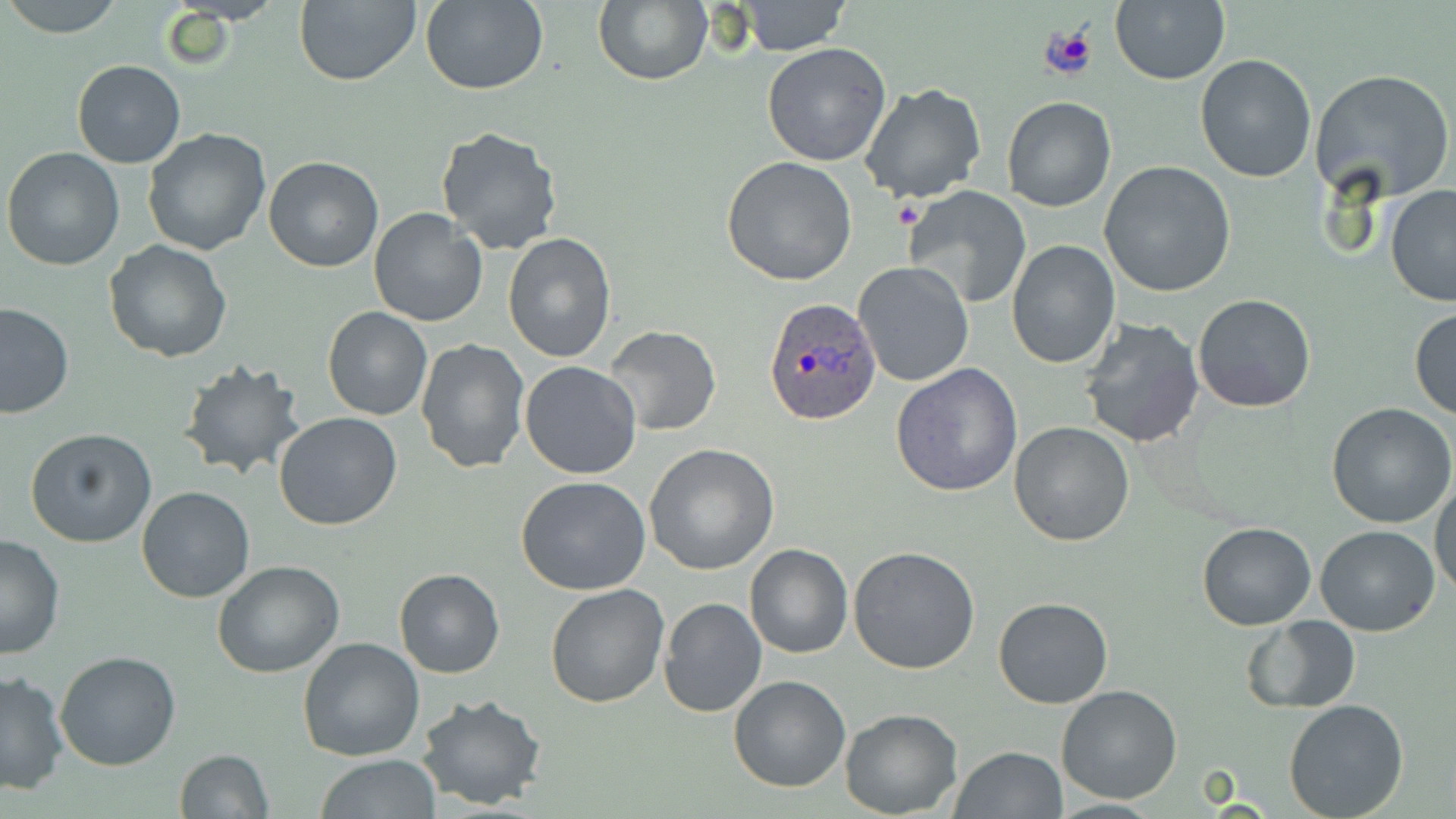
Approximate bounding boxes as [x1, y1, x2, y2] in pixels. Uninfected red blood cell locations: [4, 0, 125, 37], [293, 0, 420, 85], [592, 0, 711, 87], [420, 1, 548, 96], [736, 1, 852, 55], [1109, 1, 1229, 84], [762, 43, 893, 167], [1194, 55, 1316, 183], [71, 59, 186, 169], [1309, 68, 1455, 204], [858, 85, 985, 205], [1001, 96, 1116, 213], [435, 125, 564, 256], [142, 128, 272, 256], [3, 146, 126, 269], [263, 156, 385, 272], [721, 156, 858, 286], [1099, 162, 1237, 297], [903, 184, 1031, 309], [1384, 185, 1456, 307], [369, 208, 489, 329], [503, 234, 616, 362], [103, 239, 232, 363], [1006, 241, 1120, 370], [854, 260, 975, 388], [1192, 292, 1316, 413], [0, 301, 76, 418], [323, 306, 432, 421], [1409, 306, 1456, 420], [1078, 316, 1205, 450], [602, 324, 722, 436], [414, 336, 530, 474], [177, 357, 309, 483], [519, 361, 642, 480], [892, 364, 1022, 498], [1327, 403, 1456, 530], [274, 411, 402, 530], [1010, 420, 1135, 546], [25, 427, 157, 548], [645, 443, 779, 576], [515, 474, 651, 595], [1431, 477, 1456, 599], [138, 486, 254, 603], [1197, 521, 1316, 631], [1314, 525, 1440, 636], [1, 535, 64, 660], [745, 543, 852, 659], [849, 546, 980, 675], [213, 560, 344, 678], [394, 568, 504, 678], [544, 583, 668, 707], [992, 597, 1113, 709], [658, 598, 767, 718], [1242, 616, 1362, 712], [296, 637, 425, 760], [54, 651, 183, 771], [1, 669, 69, 794], [728, 674, 851, 792], [1056, 685, 1184, 804], [414, 692, 548, 809], [1283, 699, 1410, 819], [839, 707, 963, 818], [951, 746, 1067, 818], [173, 749, 275, 819], [316, 754, 440, 818]. Plasmodium ovale-infected red blood cell locations: [764, 298, 881, 426]. Slide-level diagnosis: Plasmodium ovale. Light microscopy. 1000x magnification. Thin blood film. One field of a larger specimen. Image is 1456×819 pixels. May-Grünwald-Giemsa stain.